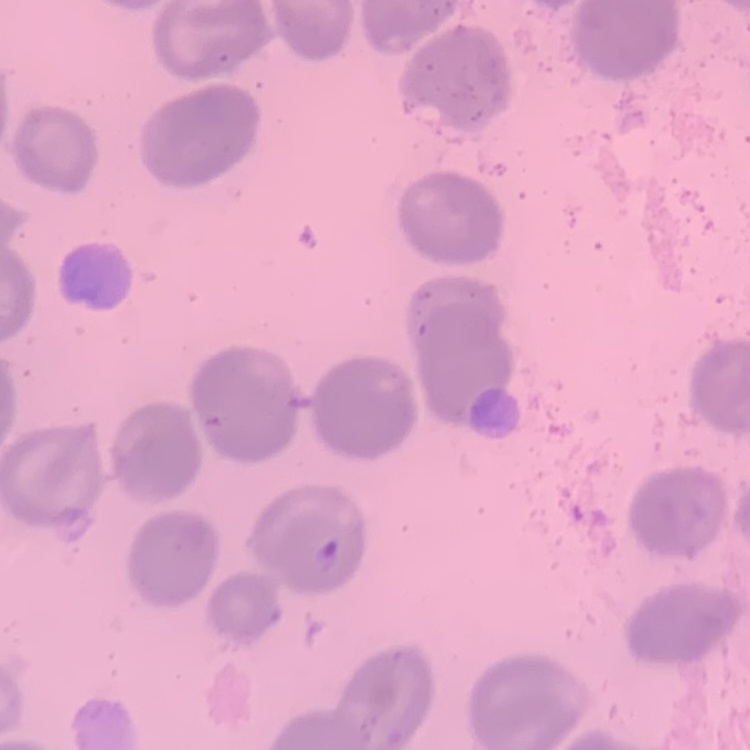 The red blood cells exhibit no rouleaux formation. One tile cut from a larger photomicrograph. Stained with either Field's or Giemsa. Thin blood smear.